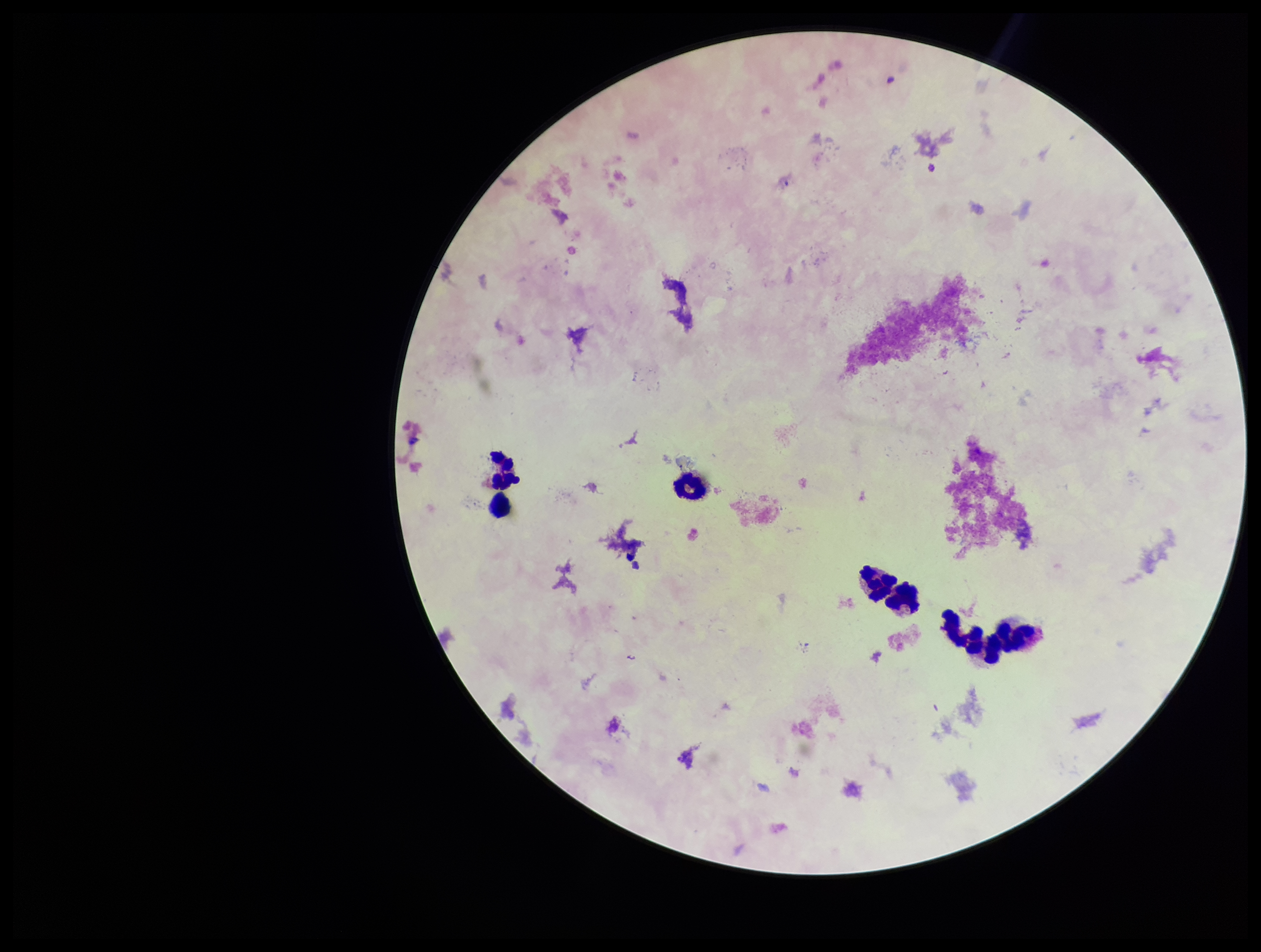
Patient malaria status: infected. One field from this slide. Preparation: thick blood smear. Species reported for this patient: Plasmodium falciparum. Parasite count: 0. Leukocyte count: 7. Stained with Giemsa. Plasmodium parasites: none detected. Image is 1261×952 pixels. Smartphone photograph taken through the eyepiece of a microscope.